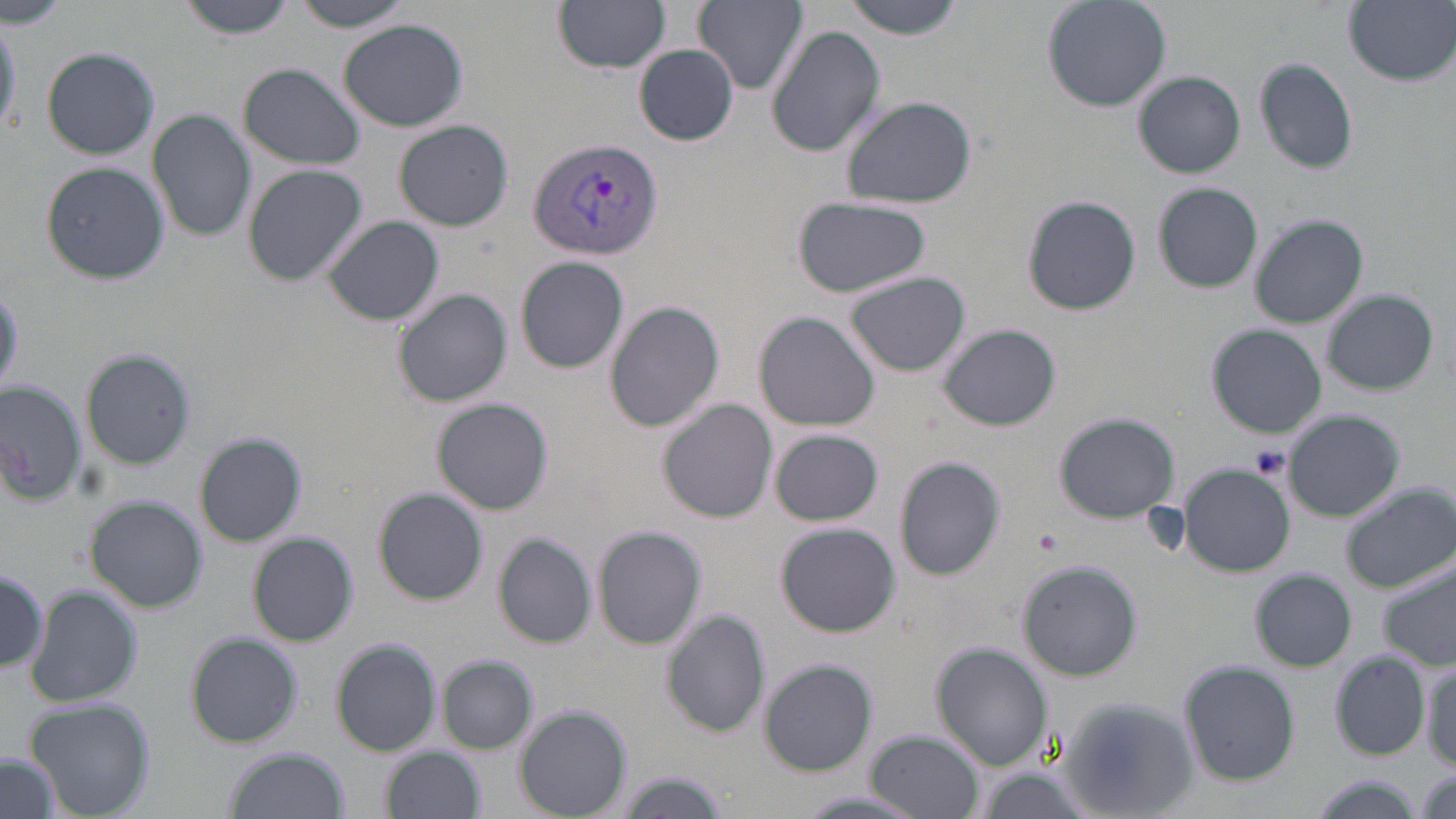
Approximate bounding boxes as (x1, y1, x2, y2) in pixels. Uninfected red blood cell locations: (1, 0, 71, 31), (177, 0, 299, 37), (554, 0, 670, 72), (695, 0, 806, 92), (840, 0, 966, 37), (1040, 0, 1171, 111), (1345, 0, 1456, 86), (288, 1, 420, 30), (0, 13, 21, 139), (338, 18, 468, 131), (766, 24, 886, 158), (636, 45, 738, 144), (41, 47, 160, 160), (1255, 59, 1358, 172), (236, 63, 365, 170), (1135, 71, 1245, 178), (840, 96, 978, 208), (148, 107, 256, 244), (395, 120, 512, 230), (40, 163, 167, 283), (242, 164, 367, 285), (1154, 183, 1263, 291), (1022, 194, 1141, 316), (791, 199, 932, 298), (1249, 213, 1369, 328), (323, 215, 444, 326), (516, 255, 629, 373), (846, 271, 969, 377), (390, 288, 512, 407), (1323, 290, 1439, 394), (605, 300, 724, 430), (753, 311, 879, 430), (939, 323, 1060, 430), (1207, 324, 1326, 437), (82, 350, 194, 469), (0, 383, 85, 503), (432, 399, 553, 514), (659, 399, 778, 522), (1285, 411, 1404, 521), (1055, 412, 1180, 523), (769, 429, 884, 526), (195, 433, 307, 547), (893, 456, 1007, 581), (1178, 464, 1294, 575), (1340, 483, 1454, 592), (373, 488, 487, 604), (85, 497, 206, 612), (774, 523, 901, 637), (592, 525, 706, 649), (247, 532, 357, 645), (493, 532, 598, 649), (1020, 560, 1142, 681), (1380, 561, 1456, 670), (0, 563, 47, 674), (1251, 570, 1355, 671), (23, 584, 143, 709), (663, 611, 770, 736), (186, 633, 303, 747), (332, 640, 441, 755), (933, 643, 1052, 771), (1330, 652, 1431, 760), (438, 654, 538, 754), (759, 659, 876, 775), (1421, 660, 1456, 770), (1181, 662, 1299, 785), (1062, 695, 1201, 818), (26, 698, 155, 819), (515, 706, 631, 816), (868, 731, 983, 818), (224, 747, 351, 819), (384, 747, 484, 818), (0, 751, 62, 819), (610, 773, 732, 816), (1301, 777, 1432, 818). Platelet locations: (1036, 530, 1064, 553). Plasmodium vivax-infected red blood cell locations: (526, 137, 665, 261). Slide-level diagnosis: Plasmodium vivax. Thin blood smear. Single field of view. Optical microscopy. May-Grünwald-Giemsa-stained preparation. Captured at 1000x magnification. Image is 1456×819 pixels.